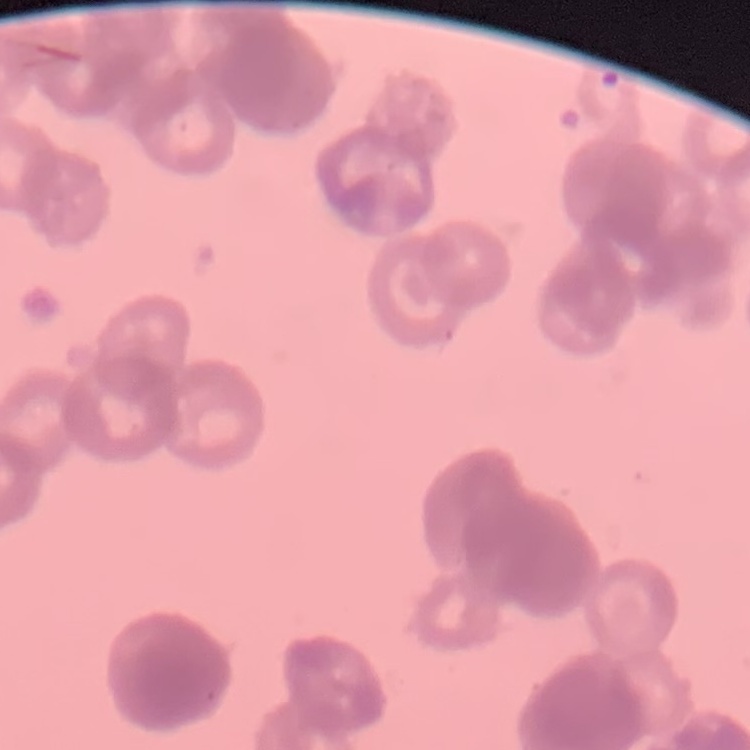
erythrocyte morphology = rouleaux formation
image type = square crop of a larger photomicrograph
preparation = thin blood film
stain = Field's or Giemsa